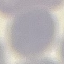
Summary:
  - Result: no malaria parasites detected
  - Image type: automatically extracted cell patch, resized to 64 × 64 pixels
  - Stain: Giemsa
  - Capture: smartphone camera at the microscope eyepiece
  - Preparation: thin blood film